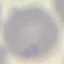

result: no malaria parasites seen
image_type: automatically extracted cell patch, resized to 64 × 64 pixels
capture: smartphone camera at the microscope eyepiece
preparation: thin blood smear
stain: Giemsa